Classify this cell by malaria status.
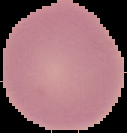
It is uninfected.

{
  "image_size": "127×133 pixels",
  "preparation": "thin blood smear",
  "image_type": "cell region segmented out of the field of view; surrounding area masked to black"
}